State the preparation type.
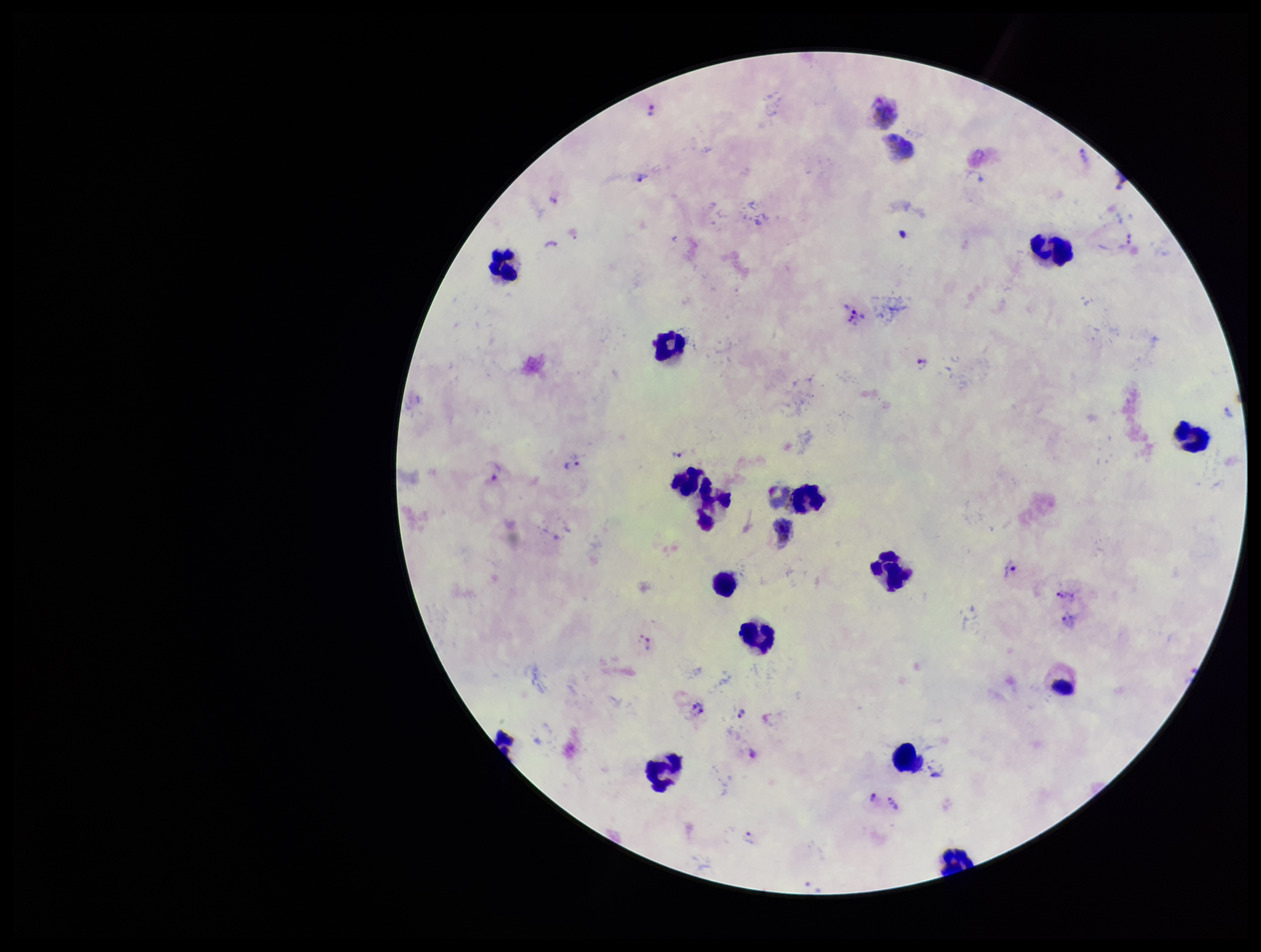
A thick smear.

Plasmodium parasites: detected. Giemsa stain. Parasite count: 19. Leukocyte count: 13. Patient malaria status: positive. One field from this slide. Photographed through the microscope eyepiece with a smartphone camera. Species reported for this patient: Plasmodium vivax. Image is 1261×952 pixels.